State which cell type is depicted.
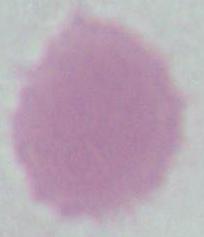

This is an erythrocyte.

1000x magnification. Photomicrograph.